Assess the morphology of the erythrocytes.
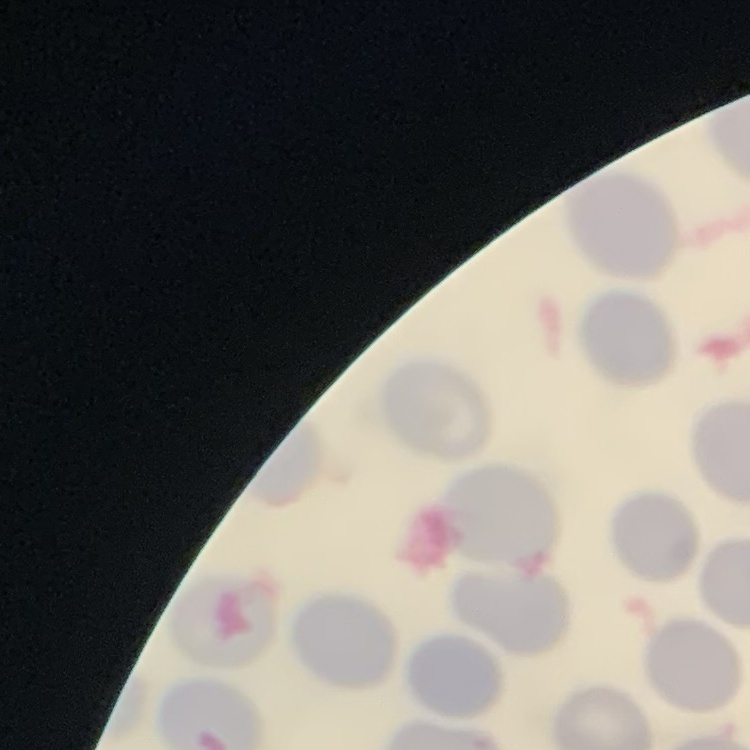

No rouleaux formation.

Thin blood film. Square crop of a larger photomicrograph. Field's or Giemsa stain.